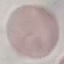

{
  "malaria_status": "uninfected",
  "preparation": "thin smear",
  "stain": "Giemsa",
  "capture": "smartphone camera at the microscope eyepiece",
  "image_type": "automatically extracted cell patch, resized to 64 × 64 pixels"
}